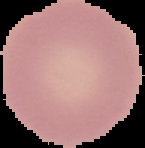

image size = 145×148 pixels
result = negative for Plasmodium parasites
image type = cell region segmented out of the field of view; surrounding area masked to black
preparation = thin blood smear